State which cell type is depicted.
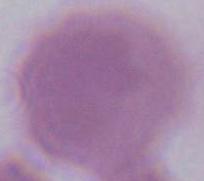
An erythrocyte.

magnification: 1000x
modality: micrograph